Locate every Plasmodium parasite.
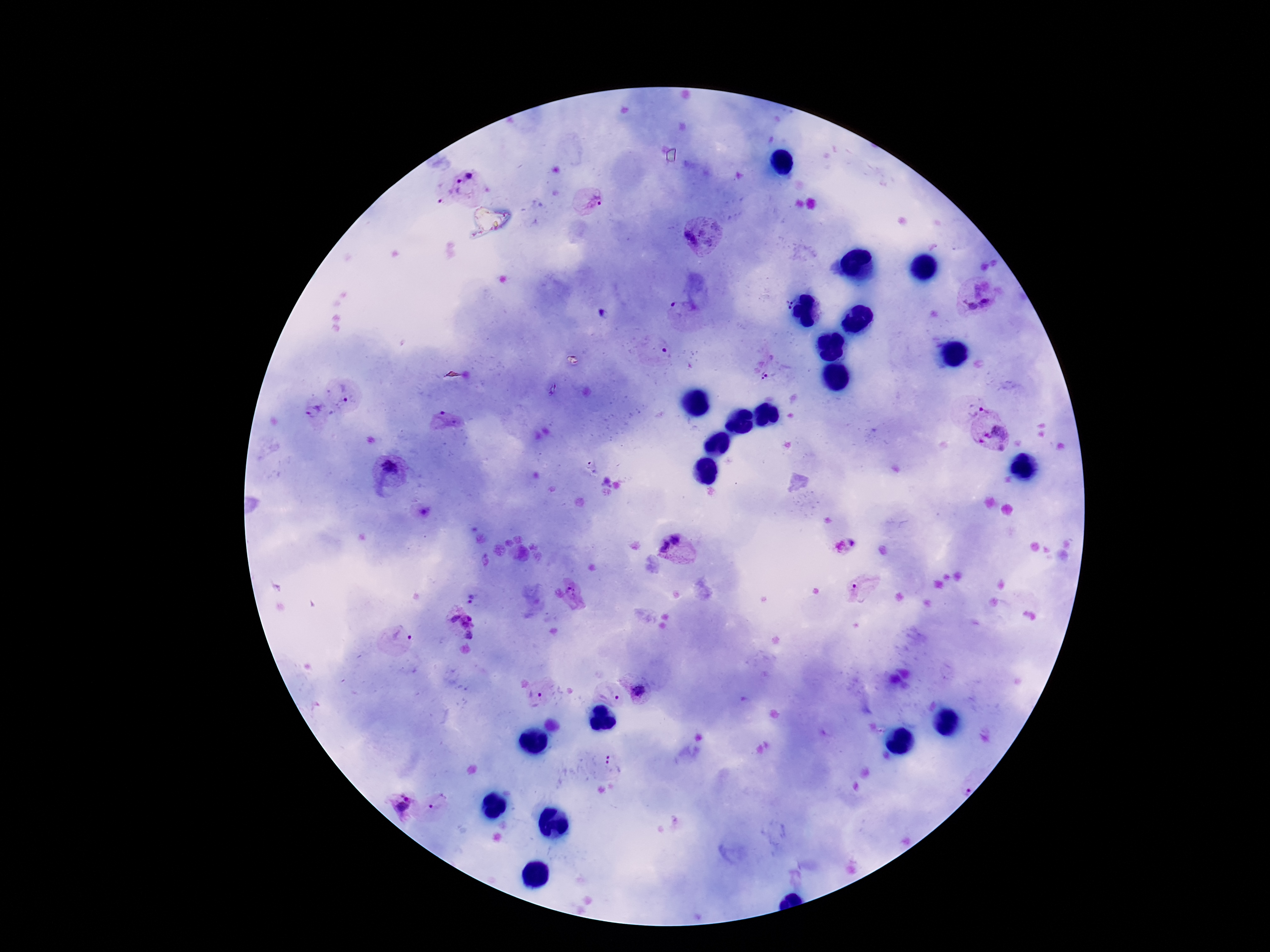
Approximate object centers, in pixels from the top-left corner.
Plasmodium parasites: (x=471, y=173), (x=460, y=189), (x=592, y=201), (x=699, y=239), (x=789, y=302), (x=985, y=303), (x=970, y=304), (x=764, y=377), (x=347, y=398), (x=974, y=405), (x=315, y=412), (x=447, y=423), (x=997, y=437), (x=387, y=465), (x=675, y=537), (x=853, y=541), (x=663, y=546), (x=855, y=590), (x=570, y=592), (x=470, y=602), (x=463, y=625), (x=401, y=633), (x=640, y=691), (x=610, y=695), (x=536, y=696), (x=615, y=765), (x=966, y=789), (x=402, y=802), (x=439, y=802).

100x magnification. Thick peripheral-blood smear. Smartphone photograph taken through the microscope eyepiece. Single field of view. Image is 1270×952 pixels. Patient malaria status: infected. Giemsa-stained preparation.